Identify the parasite.
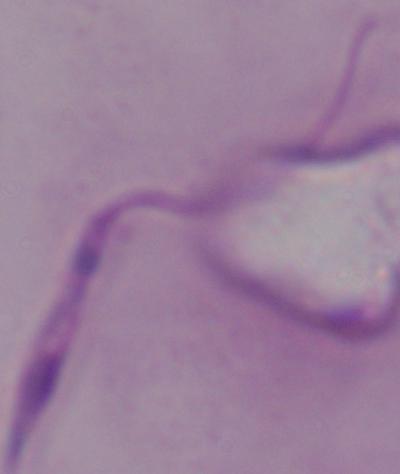

Leishmania.

magnification: 1000x
modality: photomicrograph